Locate every Trypanosoma brucei.
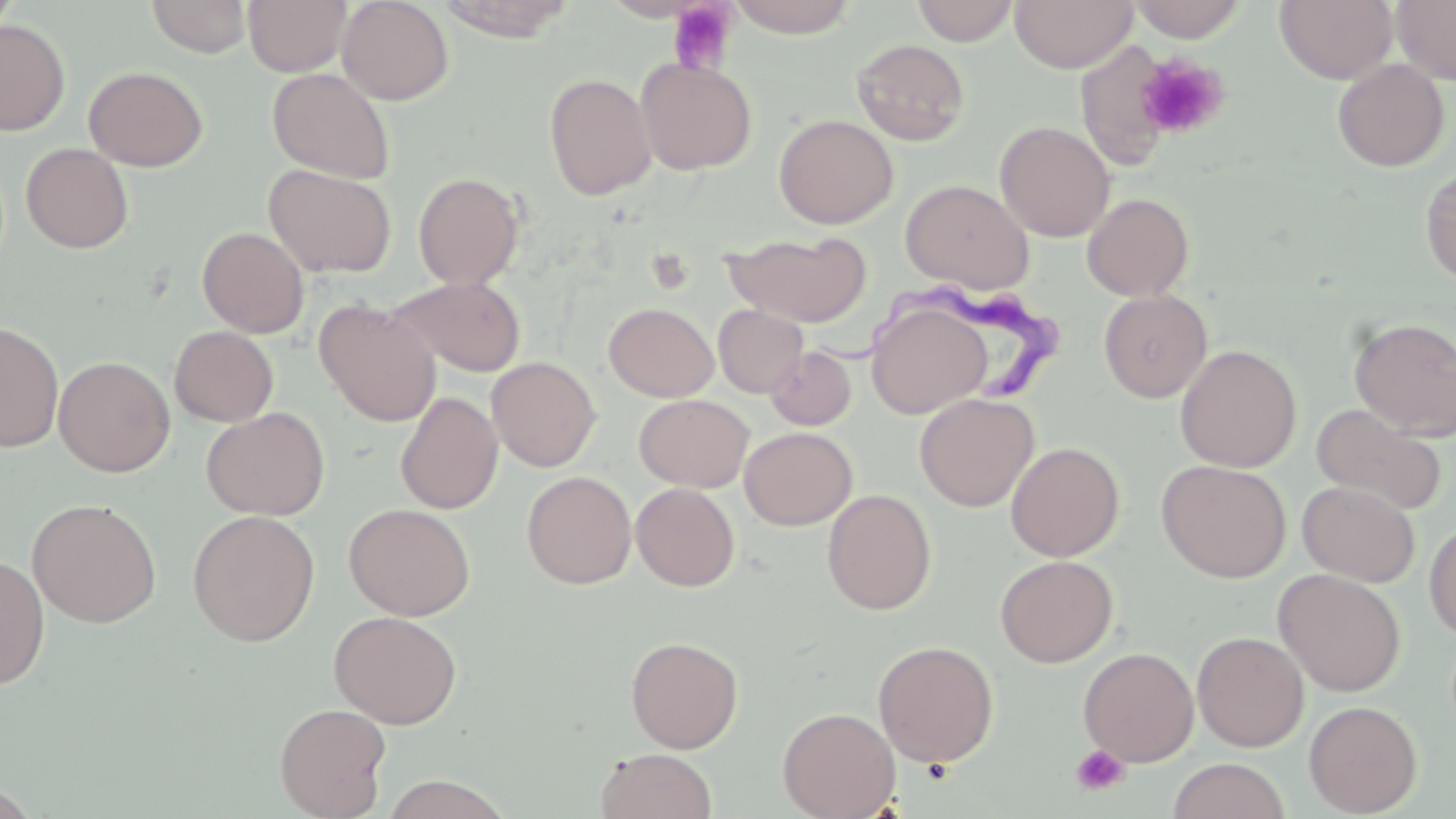
Approximate bounding boxes as (x1, y1, x2, y2) in pixels.
Trypanosoma brucei: (815, 282, 1071, 404).

Uninfected red blood cell locations: (146, 0, 252, 57), (243, 0, 351, 76), (337, 0, 454, 105), (435, 0, 577, 41), (911, 0, 1019, 46), (1010, 0, 1137, 72), (1275, 0, 1397, 84), (1393, 0, 1456, 85), (722, 1, 862, 37), (1127, 1, 1249, 42), (0, 19, 70, 135), (851, 38, 970, 146), (635, 57, 757, 175), (1332, 58, 1450, 172), (83, 66, 209, 172), (267, 67, 396, 184), (544, 72, 657, 200), (773, 113, 898, 229), (995, 121, 1115, 242), (20, 143, 133, 254), (263, 163, 396, 278), (1420, 163, 1456, 286), (413, 171, 524, 289), (899, 179, 1033, 294), (1082, 193, 1194, 300), (197, 226, 309, 338), (723, 231, 871, 326), (391, 277, 527, 377), (1098, 290, 1213, 403), (315, 299, 440, 427), (604, 302, 718, 402), (866, 302, 991, 419), (713, 305, 808, 398), (1350, 317, 1456, 440), (0, 320, 64, 453), (169, 326, 278, 427), (1175, 344, 1302, 472), (765, 345, 856, 431), (54, 355, 175, 477), (486, 357, 601, 472), (395, 391, 503, 514), (915, 392, 1039, 512), (634, 394, 754, 492), (1311, 402, 1447, 516), (201, 406, 330, 520), (739, 427, 856, 530), (1005, 441, 1125, 561), (1156, 460, 1292, 582), (521, 471, 637, 589), (1297, 481, 1419, 585), (631, 483, 740, 591), (822, 488, 937, 615), (26, 497, 162, 628), (344, 503, 475, 620), (186, 510, 321, 646), (1424, 520, 1456, 642), (0, 555, 50, 689), (994, 555, 1118, 667), (1273, 569, 1406, 696), (328, 610, 463, 728), (1192, 631, 1308, 751), (625, 635, 743, 753), (872, 640, 999, 767), (1078, 646, 1199, 766), (1303, 700, 1422, 816), (274, 702, 391, 819), (777, 706, 901, 819), (595, 748, 718, 819), (1167, 758, 1291, 819), (379, 774, 513, 818), (0, 779, 43, 817). Platelet locations: (667, 2, 739, 75), (1135, 52, 1229, 141), (1072, 744, 1129, 796). Slide-level diagnosis: Trypanosoma brucei. Thin blood film. 1000x magnification. Image is 1456×819 pixels. May-Grünwald-Giemsa-stained preparation. Single field of view. Optical microscopy.